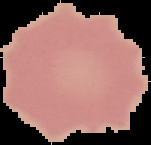
image type = segmented cell region on a black background
image size = 151×145 pixels
result = no malaria parasites detected
preparation = thin blood film